Assess for malaria.
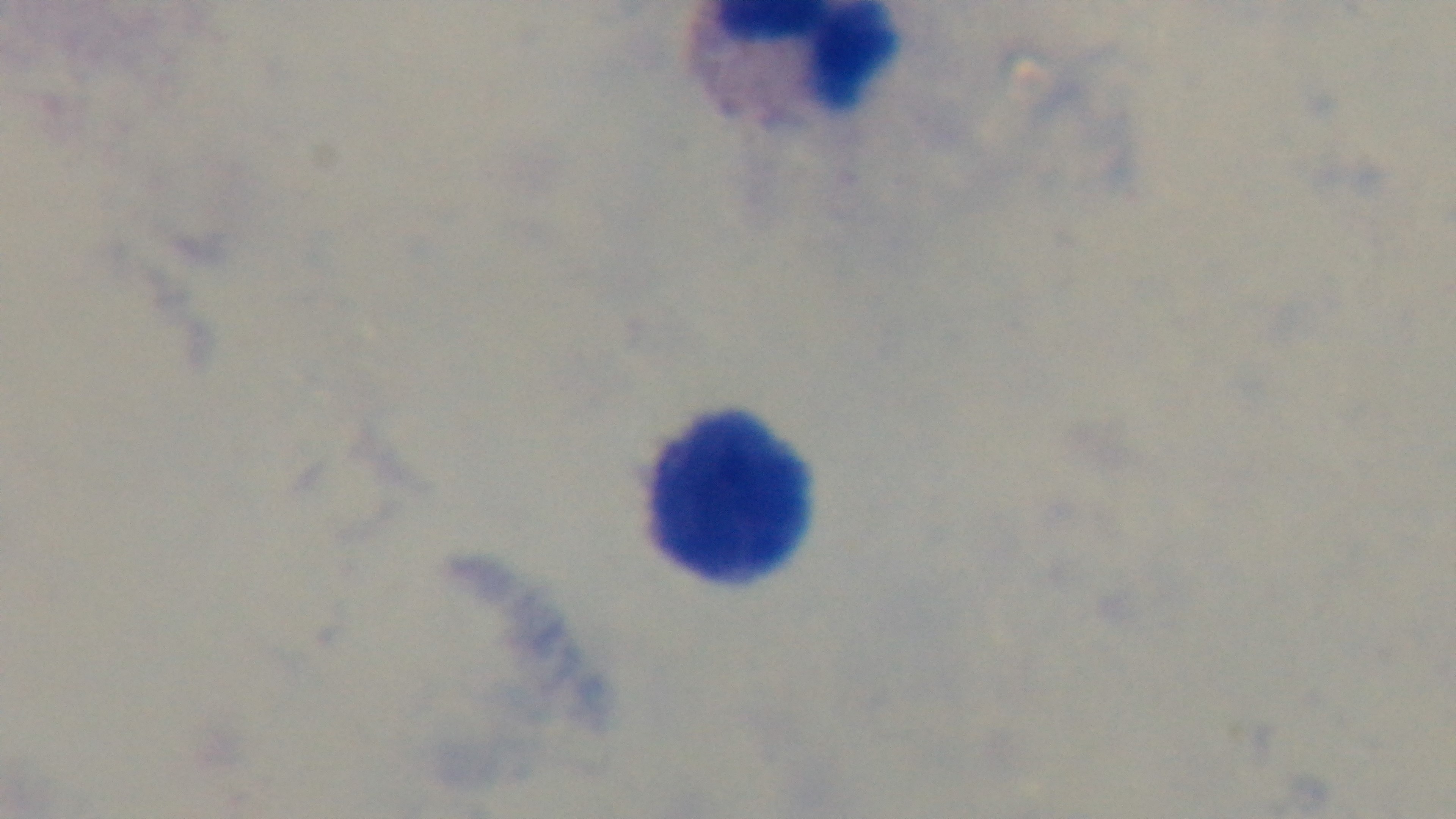
Uninfected.

Captured with a mounted 4K digital camera. Giemsa stain. Preparation: thick blood film. Light microscopy. One field from the slide. Oil-immersion objective, 100x.